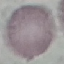

Summary:
  - Result: negative for malaria parasites
  - Capture: smartphone camera at the microscope eyepiece
  - Image type: automatically extracted cell patch, resized to 64 × 64 pixels
  - Stain: Giemsa
  - Preparation: thin blood smear